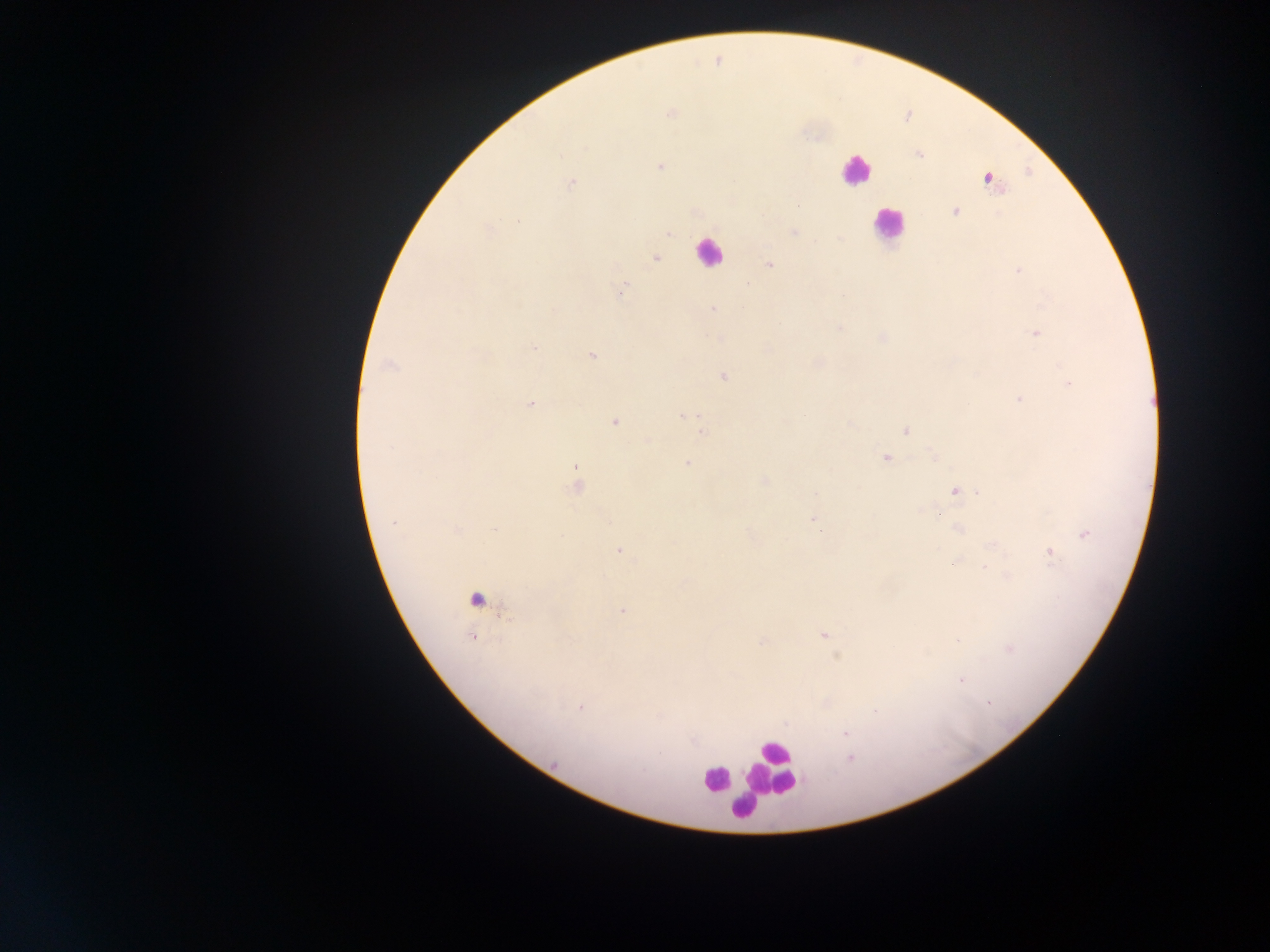

Approximate centers as (x, y) in pixels.
Summary:
  - Leukocyte locations: (855, 170), (887, 224), (708, 252), (478, 598), (771, 767), (713, 780), (745, 807)
  - Plasmodium parasite locations: (671, 113), (918, 153), (660, 167), (988, 178), (571, 183), (798, 206), (955, 211), (518, 221), (488, 230), (794, 232), (670, 234), (655, 258), (769, 265), (1017, 270), (623, 289), (713, 309), (554, 310), (840, 328), (1036, 334), (883, 337), (533, 348), (591, 356), (389, 365), (723, 377), (1069, 383), (1019, 399), (530, 404), (683, 414), (804, 415), (614, 422), (906, 431), (701, 432), (885, 458), (687, 463), (575, 467), (764, 481), (577, 485), (956, 490), (980, 492), (937, 513), (815, 521), (394, 522), (958, 529), (457, 530), (495, 530), (1085, 534), (619, 551), (1050, 555), (953, 563), (984, 567), (621, 611), (824, 635), (472, 638), (763, 641), (1010, 649), (961, 680), (988, 704), (581, 707), (876, 712), (845, 732), (851, 759), (555, 763)
  - Image size: 1270×952 pixels
  - Preparation: thick blood film
  - Country: Ghana
  - Capture: mobile-phone photograph through a microscope
  - Field of view: single